Report the malaria status of this cell.
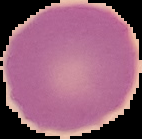
It is uninfected.

{
  "preparation": "thin blood film",
  "image_type": "segmented cell region on a black background",
  "image_size": "142×139 pixels"
}